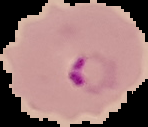

Summary:
  - Preparation: thin blood smear
  - Image size: 148×127 pixels
  - Image type: segmented cell region on a black background
  - Malaria status: parasitized